Classify this cell by malaria status.
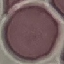

It is uninfected.

Giemsa stain. Acquired by smartphone through the microscope eyepiece. Thin blood smear. Cell patch, automatically extracted from a larger field of view and resized to 64 × 64 pixels.